Identify the parasite.
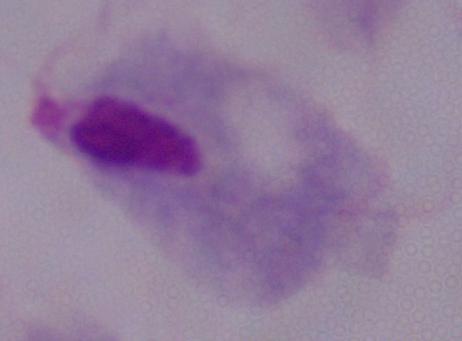
A trichomonad.

Captured at 1000x magnification. Micrograph.